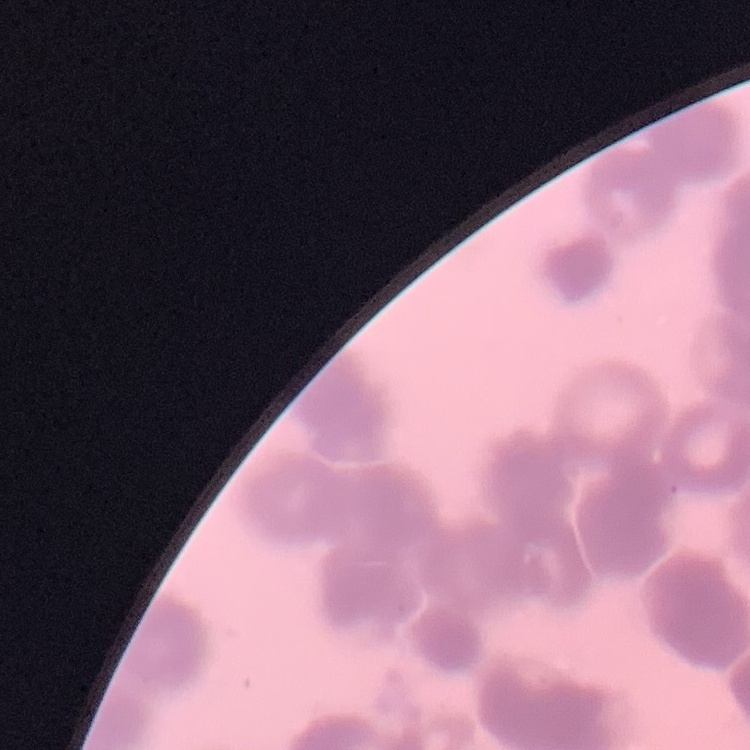

Summary:
  - Red blood cell morphology: rouleaux formation
  - Stain: Field's or Giemsa
  - Image type: square crop of a larger photomicrograph
  - Preparation: thin peripheral smear